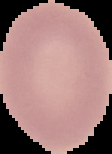

result = no malaria parasites detected
image size = 112×154 pixels
preparation = thin blood film
image type = segmented cell region with the area outside set to black